Describe the morphology of the erythrocytes.
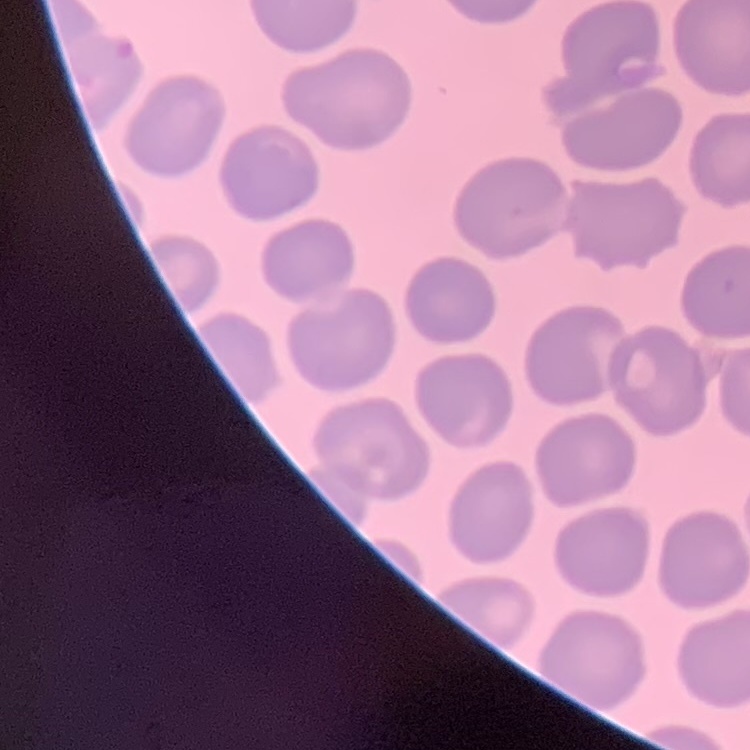
They show no rouleaux formation.

Thin peripheral smear. Field's or Giemsa stain. Square crop of a larger photomicrograph.